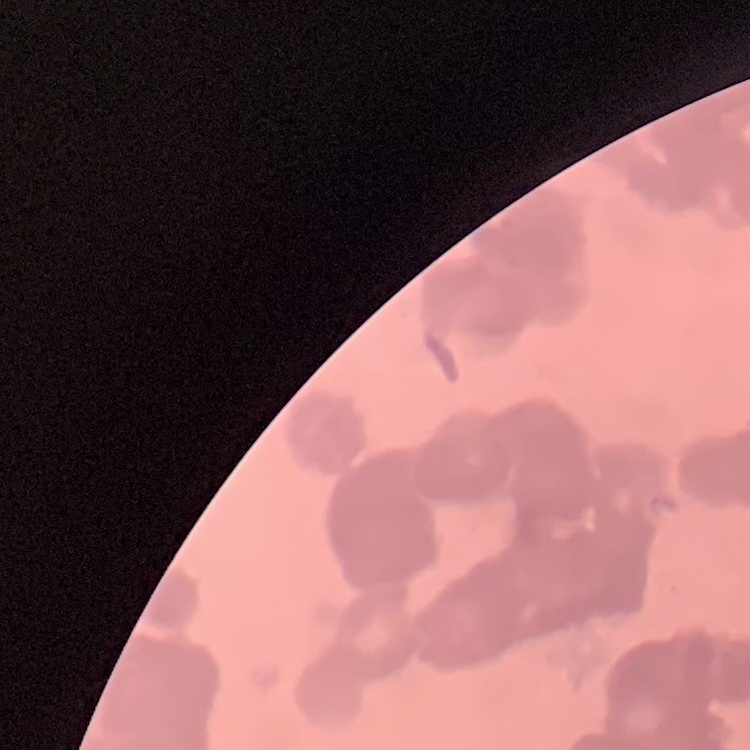 The red blood cells show rouleaux formation. Field's or Giemsa stain. Thin peripheral smear. Square crop of a larger photomicrograph.